Identify the blood parasite species.
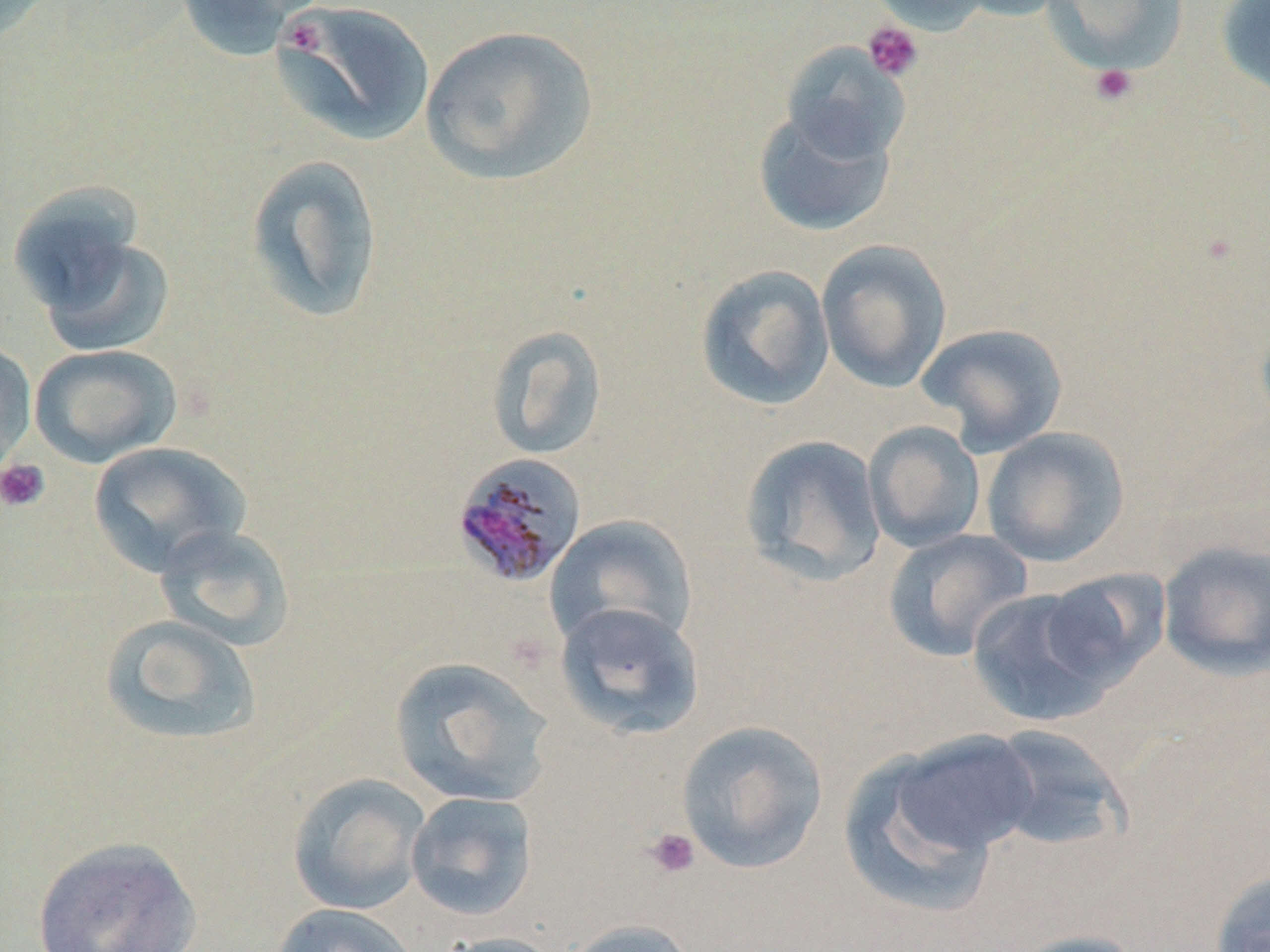
Plasmodium malariae.

Approximate bounding boxes as (x1, y1, x2, y2) in pixels. Platelet locations: (281, 17, 328, 59), (863, 20, 923, 82), (1089, 64, 1138, 107), (0, 458, 50, 513), (643, 827, 701, 880). Uninfected red blood cell locations: (0, 0, 57, 46), (172, 0, 324, 62), (866, 0, 994, 34), (948, 0, 1075, 22), (1041, 0, 1188, 75), (1215, 1, 1270, 99), (273, 2, 436, 147), (418, 25, 599, 188), (779, 40, 911, 165), (752, 105, 897, 237), (244, 153, 385, 325), (7, 182, 148, 318), (33, 232, 176, 358), (816, 239, 952, 393), (695, 264, 835, 412), (916, 322, 1069, 457), (484, 324, 609, 461), (0, 339, 37, 477), (29, 344, 182, 468), (863, 421, 986, 553), (981, 426, 1130, 568), (738, 434, 887, 587), (88, 441, 252, 577), (544, 514, 698, 650), (153, 523, 295, 651), (882, 528, 1033, 663), (1157, 541, 1270, 680), (1038, 567, 1171, 691), (966, 586, 1121, 728), (554, 601, 704, 740), (98, 614, 262, 747), (388, 656, 556, 807), (675, 720, 829, 874), (982, 723, 1133, 857), (881, 729, 1042, 868), (839, 744, 1010, 917), (286, 772, 431, 915), (405, 790, 539, 921), (30, 835, 204, 951), (1209, 869, 1270, 952), (270, 902, 421, 952), (560, 919, 700, 952), (1005, 930, 1150, 952), (433, 932, 568, 952). Plasmodium malariae-infected red blood cell locations: (451, 451, 588, 589). May-Grünwald-Giemsa stain. Single field of view. Captured at 1000x magnification. Image is 1270×952 pixels. Thin blood film. Optical microscopy.